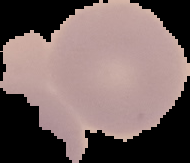

Summary:
  - Image type: segmented cell region with the area outside set to black
  - Malaria status: uninfected
  - Image size: 190×163 pixels
  - Preparation: thin blood film